Identify the parasite.
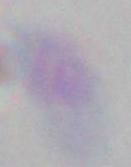
This is Toxoplasma gondii.

Captured at 1000x magnification. Photomicrograph.